Name the cell type shown.
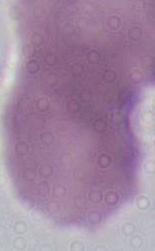

An erythrocyte.

modality = micrograph
magnification = 1000x